State which parasite is depicted.
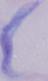
This is a trypanosome.

modality = photomicrograph
magnification = 1000x